Locate every Plasmodium vivax-infected red blood cell.
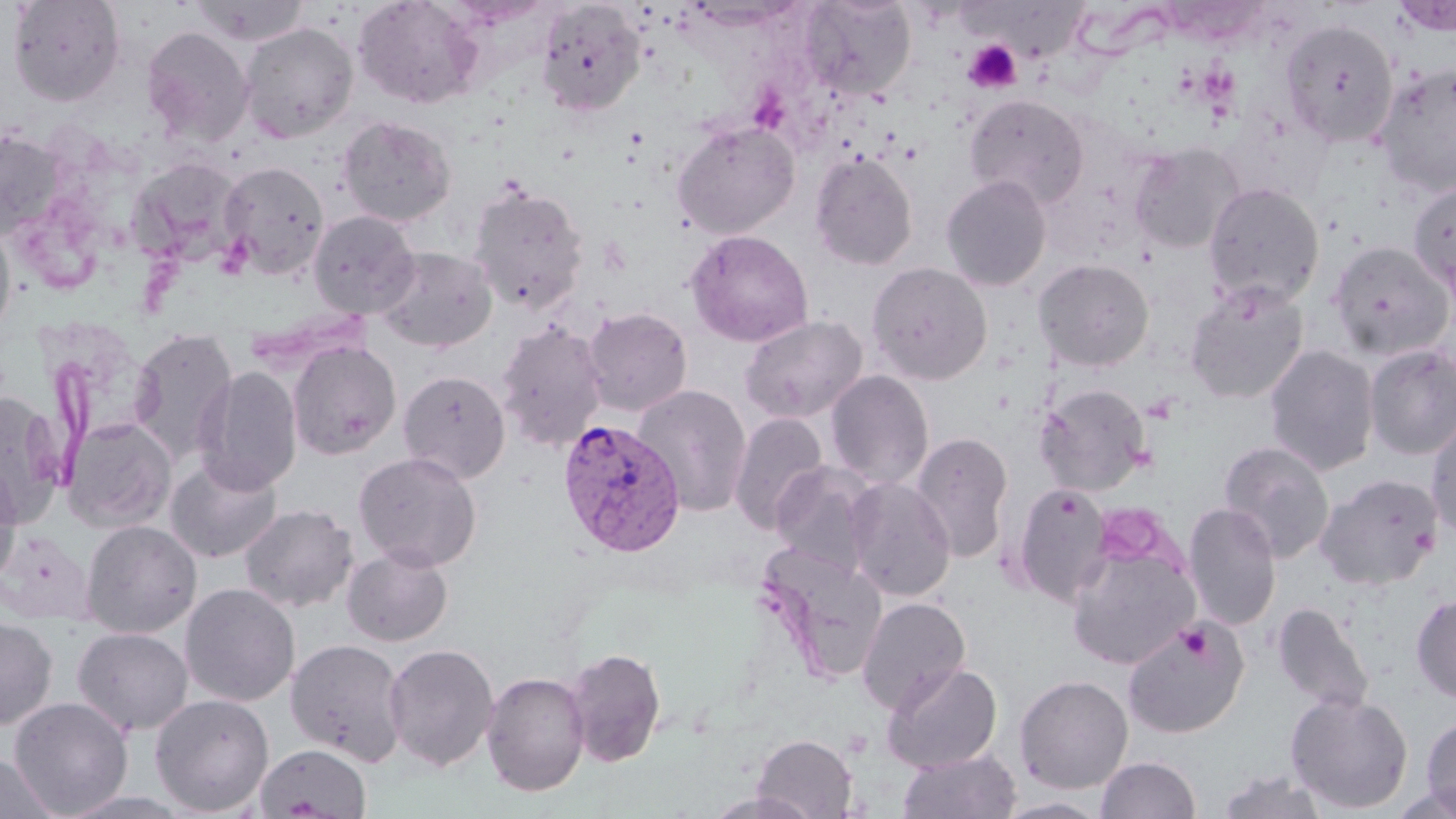

Approximate bounding boxes as [x1, y1, x2, y2] in pixels.
Plasmodium vivax-infected red blood cells: [557, 419, 687, 558].

slide-level diagnosis = Plasmodium vivax
uninfected red blood cell locations = approximate bounding boxes as [x1, y1, x2, y2] in pixels: [7, 0, 126, 106], [191, 0, 310, 46], [352, 0, 483, 109], [799, 0, 917, 100], [1392, 0, 1455, 37], [536, 1, 645, 117], [1280, 19, 1399, 146], [239, 22, 359, 144], [140, 25, 254, 147], [1372, 64, 1456, 197], [964, 94, 1090, 210], [337, 116, 456, 227], [672, 119, 801, 239], [0, 127, 70, 240], [1129, 141, 1244, 254], [809, 152, 918, 270], [127, 157, 245, 266], [218, 160, 330, 280], [941, 174, 1052, 291], [1407, 181, 1456, 302], [469, 182, 589, 315], [1203, 182, 1324, 309], [308, 210, 421, 319], [0, 220, 17, 341], [685, 229, 813, 347], [1328, 241, 1453, 360], [374, 246, 499, 353], [1033, 258, 1154, 372], [866, 262, 993, 385], [1185, 281, 1309, 405], [581, 307, 693, 417], [739, 315, 867, 423], [496, 321, 608, 451], [129, 328, 239, 463], [287, 341, 401, 460], [1263, 344, 1380, 475], [1364, 345, 1456, 460], [194, 366, 303, 495], [398, 370, 511, 484], [825, 370, 935, 490], [1035, 383, 1152, 496], [632, 384, 754, 517], [0, 390, 66, 527], [729, 412, 830, 534], [1425, 413, 1456, 541], [62, 416, 177, 533], [910, 432, 1014, 562], [1218, 441, 1335, 563], [354, 452, 482, 572], [165, 456, 283, 563], [0, 460, 22, 588], [770, 461, 883, 579], [1315, 473, 1444, 590], [843, 476, 956, 601], [1012, 484, 1111, 606], [239, 503, 358, 613], [1182, 503, 1282, 631], [81, 519, 203, 637], [1065, 539, 1200, 670], [342, 546, 453, 647], [755, 548, 888, 685], [180, 583, 300, 706], [1411, 594, 1456, 702], [856, 596, 971, 713], [1272, 602, 1374, 715], [0, 617, 58, 730], [1122, 618, 1249, 737], [72, 627, 193, 735], [285, 638, 408, 767], [383, 643, 500, 771], [563, 647, 666, 767], [881, 662, 1002, 772], [481, 671, 590, 797], [1014, 674, 1133, 794], [1286, 692, 1413, 814], [150, 694, 275, 816], [8, 696, 134, 817], [1421, 714, 1456, 817], [751, 733, 859, 818], [254, 743, 371, 818], [897, 747, 1021, 819], [0, 751, 57, 819], [1096, 756, 1200, 818], [1215, 770, 1331, 819], [58, 790, 194, 819], [704, 791, 820, 819], [996, 797, 1109, 818]
platelet locations = approximate bounding boxes as [x1, y1, x2, y2] in pixels: [964, 40, 1022, 93], [1178, 624, 1211, 662]
field of view = one of a larger specimen
modality = light microscopy
magnification = 1000x
image size = 1456×819 pixels
preparation = thin blood smear
stain = May-Grünwald-Giemsa